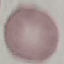
Result: negative for malaria parasites. Automatically extracted cell patch, resized to 64 × 64 pixels. Photographed with a smartphone camera at the microscope eyepiece. Thin smear of blood. Giemsa-stained preparation.